Assess the morphology of the erythrocytes.
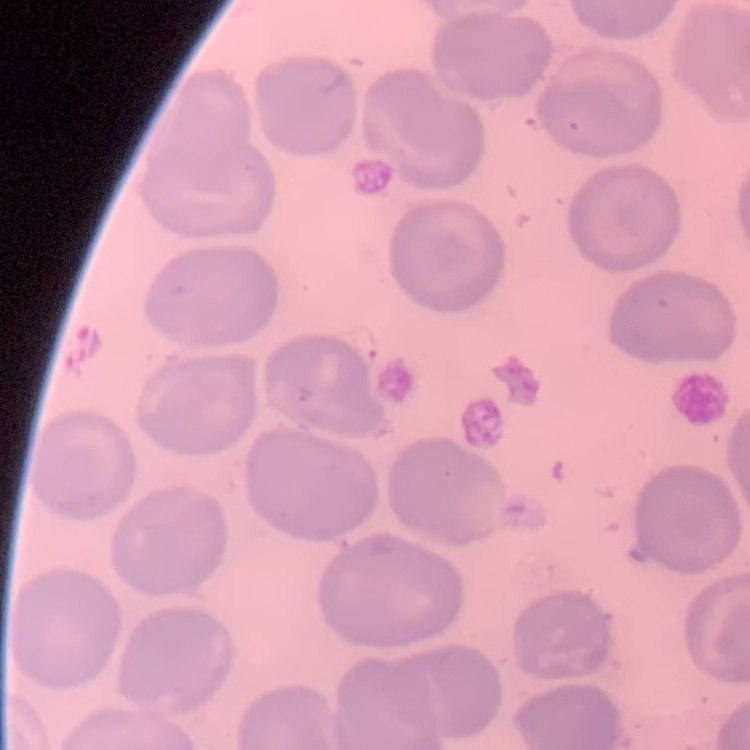
They show no rouleaux formation.

One tile cut from a larger photomicrograph. Thin blood smear. Stained with either Field's or Giemsa.